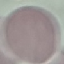

Result: negative for malaria parasites. Acquired by smartphone through the microscope eyepiece. Automatically extracted cell patch, resized to 64 × 64 pixels. Thin smear of blood. Giemsa-stained preparation.